Name the cell type shown.
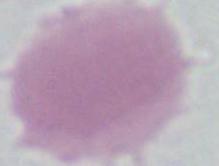

An erythrocyte.

Captured at 1000x magnification. Micrograph.